Locate every Plasmodium parasite.
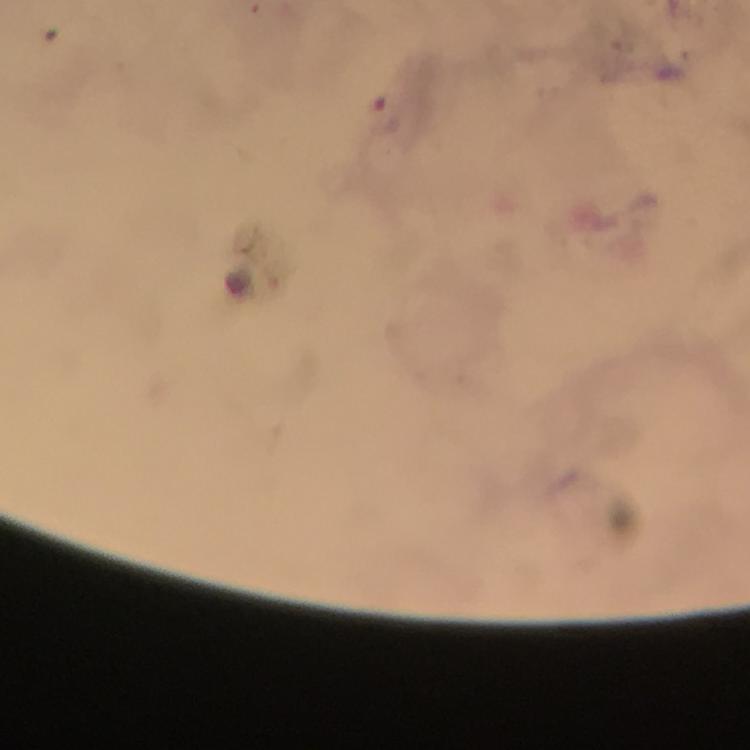

Approximate centers as [x, y] in pixels.
Plasmodium parasites: [389, 115].

magnification = 100x
context = from a malaria diagnostic workup
cropped from = a single field of view
capture = smartphone camera through the microscope
image size = 750×750 pixels
immersion oil = applied
preparation = thick smear
stain = Giemsa